Report the malaria status of this cell.
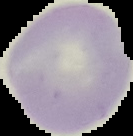
Uninfected.

Image is 133×136 pixels. The area outside the segmented cell region is set to black. From a thin blood smear.